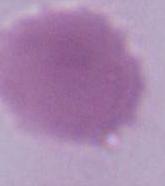

Micrograph. An erythrocyte is seen. 1000x magnification.